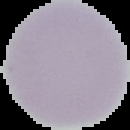
Malaria status: uninfected. Image is 130×130 pixels. Cell region segmented out of the field of view; the surrounding area is masked to black. From a thin blood film.